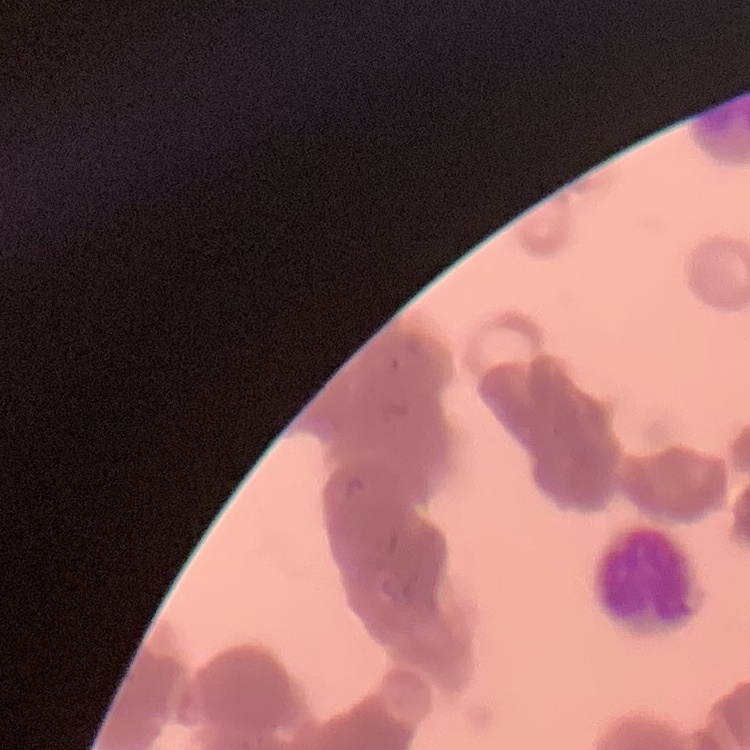

Summary:
  - Red blood cell morphology: rouleaux formation
  - Preparation: thin peripheral smear
  - Image type: one tile cut from a larger photomicrograph
  - Stain: Field's or Giemsa